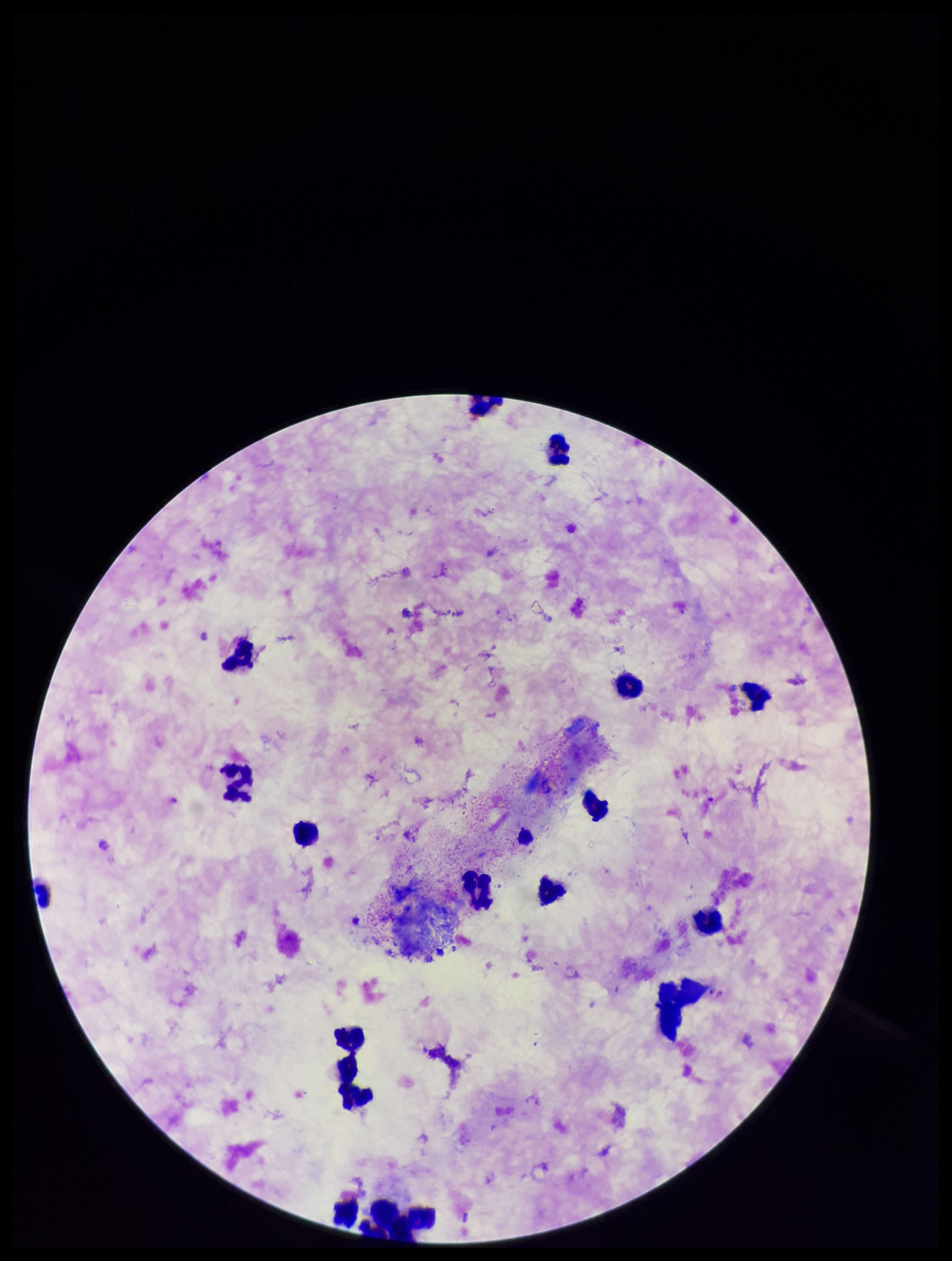

Summary:
  - Patient malaria status: positive
  - Plasmodium parasites: none detected
  - Image size: 952×1261 pixels
  - Stain: Giemsa
  - Parasite count: 0
  - Species reported for this patient: Plasmodium falciparum
  - Field of view: one from this slide
  - Preparation: thick
  - Leukocyte count: 17
  - Capture: smartphone photograph through the microscope eyepiece